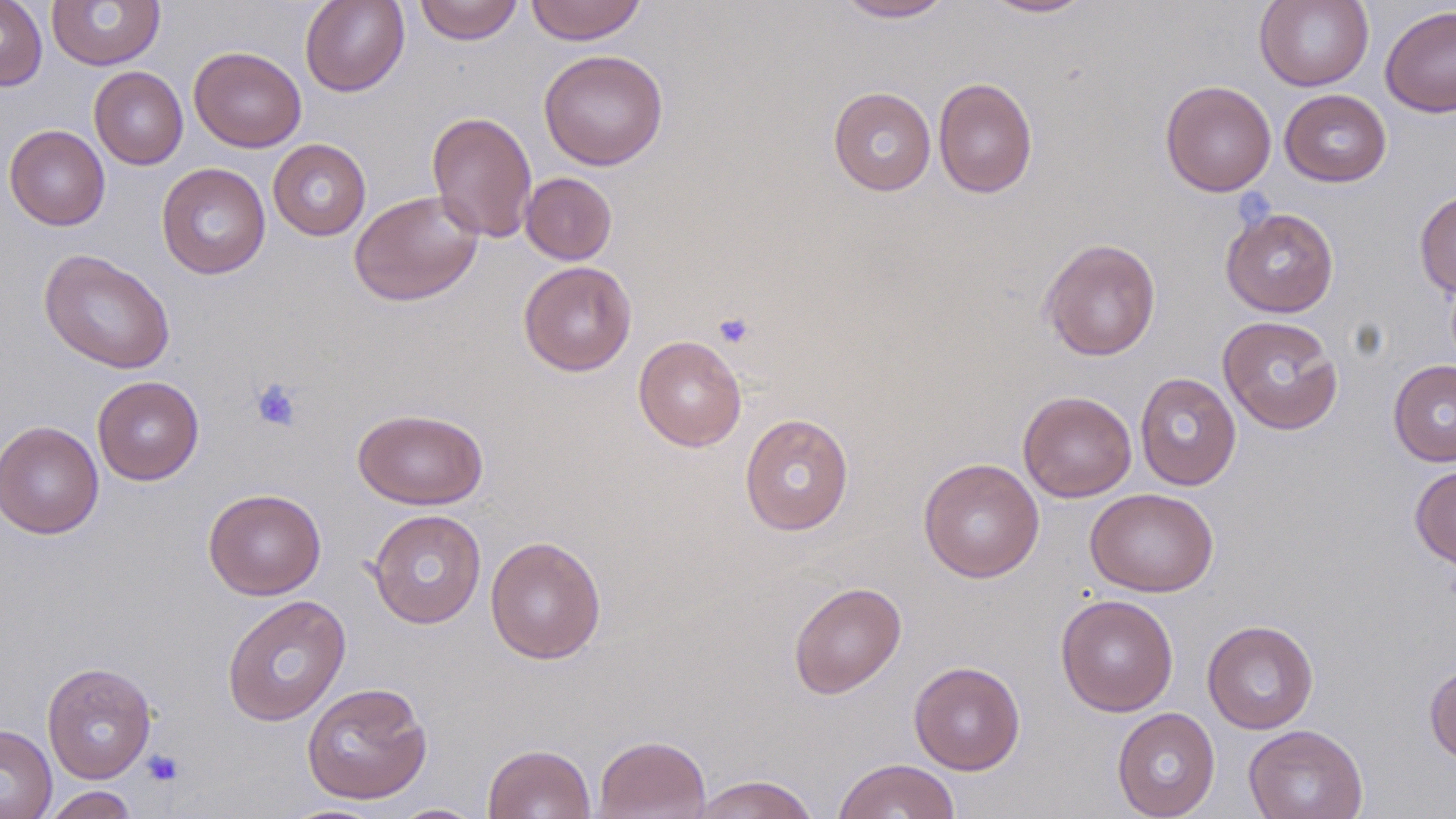

slide-level diagnosis = negative for blood parasites
uninfected red blood cell locations = approximate bounding boxes as (x1,y1)-(x2,y2) corner pairs in pixels: (0,0)-(47,91), (300,0)-(410,96), (414,0)-(524,45), (525,0)-(647,45), (836,0)-(956,22), (982,0)-(1095,18), (1254,0)-(1374,91), (46,1)-(165,70), (1379,5)-(1456,118), (189,46)-(306,152), (538,49)-(669,170), (89,66)-(188,169), (933,77)-(1038,198), (1160,80)-(1277,196), (828,86)-(936,196), (1280,89)-(1392,187), (426,110)-(538,243), (4,124)-(110,231), (268,139)-(371,241), (156,162)-(270,279), (520,172)-(618,265), (1414,188)-(1456,299), (349,189)-(484,306), (1220,207)-(1339,317), (1039,238)-(1161,361), (39,248)-(176,374), (518,261)-(637,376), (1217,315)-(1344,435), (633,335)-(747,452), (1388,359)-(1456,467), (1135,372)-(1241,490), (92,376)-(204,485), (1018,390)-(1137,502), (352,407)-(488,510), (739,413)-(854,536), (1,420)-(104,539), (918,457)-(1044,583), (1410,464)-(1456,571), (1085,487)-(1219,597), (203,488)-(326,600), (367,509)-(486,628), (485,536)-(607,664), (788,581)-(906,698), (1056,594)-(1179,716), (221,595)-(351,726), (1202,619)-(1319,734), (41,661)-(157,784), (909,661)-(1026,775), (1424,661)-(1456,765), (301,681)-(432,805), (1112,707)-(1220,818), (0,724)-(57,819), (1243,724)-(1368,819), (593,734)-(710,818), (483,743)-(595,819), (832,758)-(961,819), (689,774)-(819,819), (39,785)-(140,818), (388,803)-(486,818)
modality = light microscopy
magnification = 1000x
stain = May-Grünwald-Giemsa
image size = 1456×819 pixels
field of view = single
preparation = thin blood smear
platelet locations = approximate bounding boxes as (x1,y1)-(x2,y2) corner pairs in pixels: (713,312)-(756,349), (250,378)-(303,432), (141,750)-(184,787)